Give the preparation type.
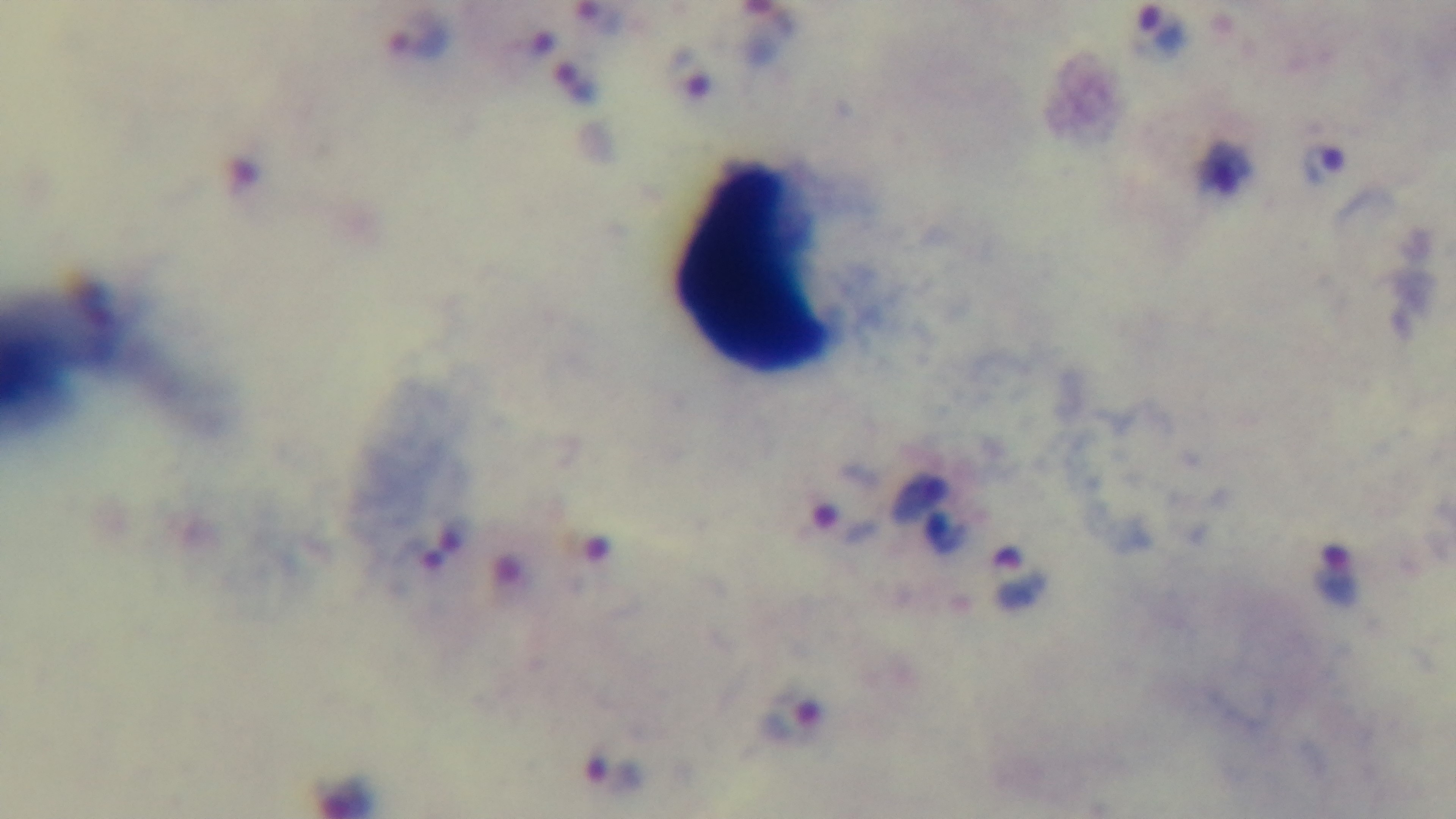

A thick smear.

Summary:
  - Malaria status: infected
  - Objective: 100x oil immersion
  - Modality: light microscopy
  - Stain: Giemsa
  - Field of view: single
  - Capture: mounted 4K digital camera